State which parasite is depicted.
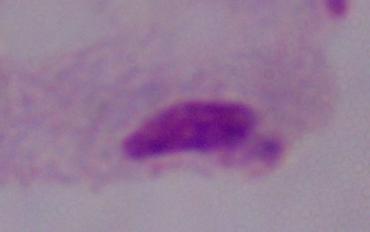

A trichomonad.

Photomicrograph. 1000x magnification.